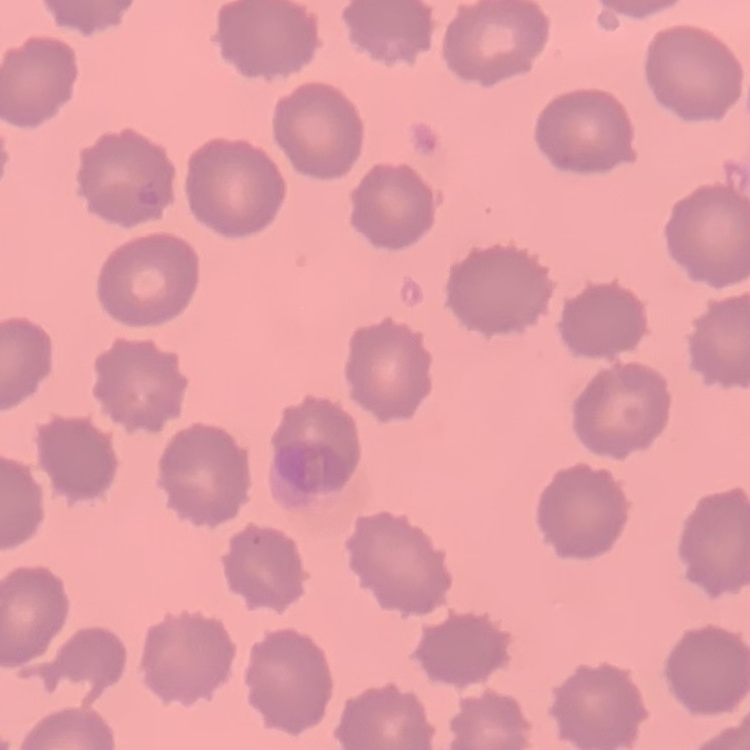

Summary:
  - Red blood cell morphology: no rouleaux formation
  - Stain: Field's or Giemsa
  - Image type: one tile cut from a larger photomicrograph
  - Preparation: thin blood film